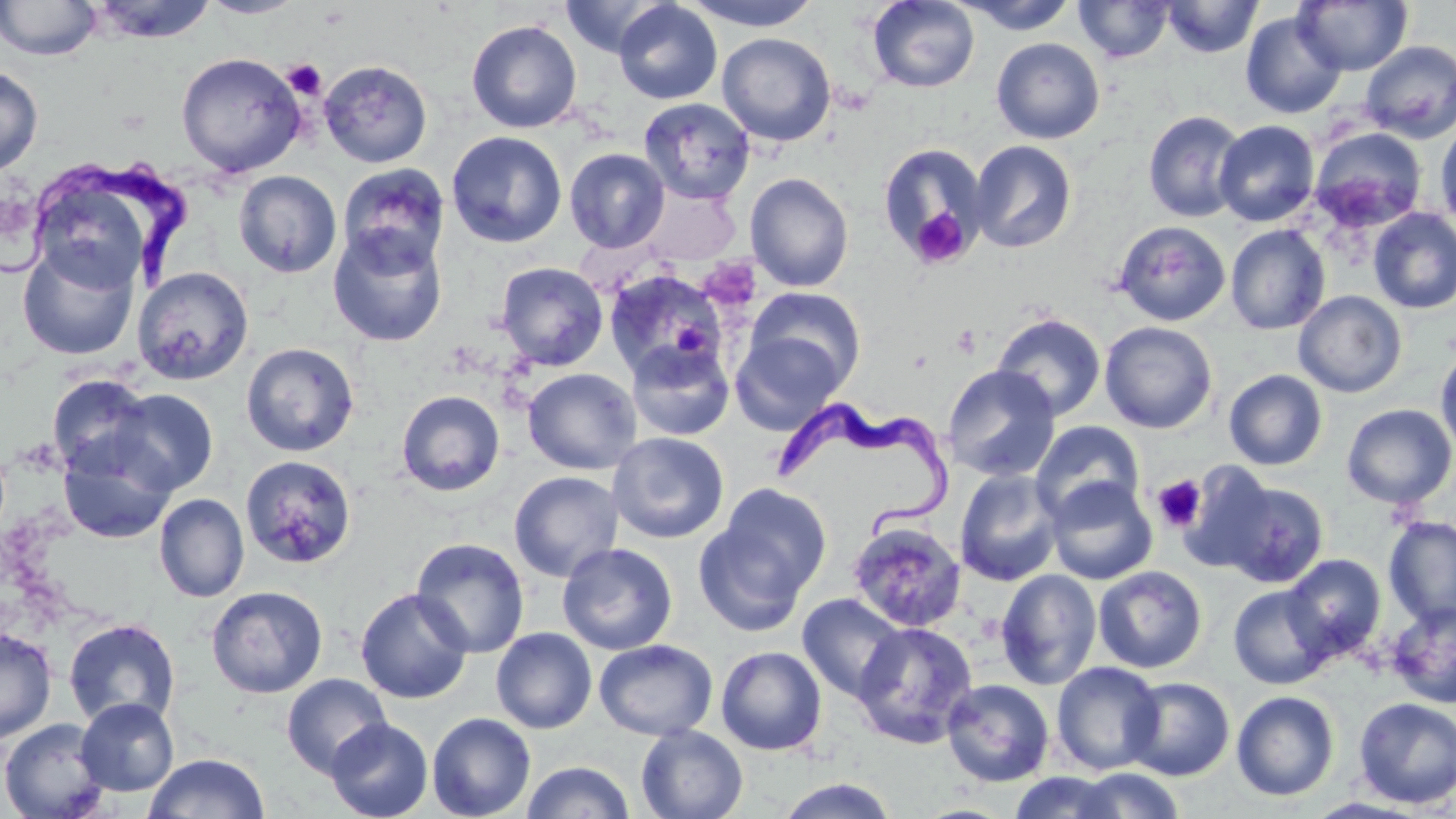
slide-level diagnosis = Trypanosoma brucei
preparation = thin blood smear
Trypanosoma brucei locations = approximate bounding boxes as [x1, y1, x2, y2] in pixels: [8, 159, 193, 293], [778, 400, 952, 542]
uninfected red blood cell locations = approximate bounding boxes as [x1, y1, x2, y2] in pixels: [0, 0, 103, 60], [87, 0, 220, 44], [197, 0, 308, 19], [561, 0, 669, 58], [685, 0, 821, 30], [1074, 0, 1175, 62], [1161, 0, 1262, 58], [614, 1, 723, 105], [867, 1, 980, 93], [952, 1, 1079, 34], [1294, 1, 1412, 74], [1240, 11, 1347, 119], [466, 19, 582, 133], [717, 32, 836, 146], [992, 38, 1105, 143], [983, 40, 1092, 254], [1359, 40, 1456, 144], [176, 52, 306, 177], [318, 59, 433, 168], [0, 66, 43, 176], [639, 97, 756, 203], [1143, 110, 1247, 223], [1213, 119, 1320, 226], [1434, 122, 1456, 230], [1310, 127, 1427, 232], [446, 130, 567, 248], [969, 140, 1077, 253], [877, 143, 989, 263], [564, 148, 670, 253], [337, 163, 450, 272], [233, 170, 342, 278], [745, 172, 854, 292], [639, 183, 740, 264], [1368, 207, 1456, 314], [1113, 220, 1230, 326], [327, 224, 448, 347], [1225, 224, 1330, 335], [17, 240, 140, 361], [495, 262, 608, 371], [132, 266, 254, 385], [604, 270, 727, 380], [745, 287, 866, 394], [1293, 290, 1407, 398], [992, 312, 1106, 421], [1100, 321, 1218, 434], [731, 332, 846, 435], [626, 339, 736, 441], [241, 342, 359, 456], [1434, 344, 1456, 458], [942, 364, 1060, 482], [522, 367, 643, 475], [1224, 369, 1328, 470], [47, 373, 158, 479], [106, 387, 218, 495], [396, 390, 505, 496], [1341, 403, 1456, 509], [1031, 421, 1144, 523], [57, 432, 177, 545], [607, 432, 729, 543], [239, 455, 357, 570], [1176, 463, 1280, 575], [954, 469, 1064, 587], [508, 470, 624, 583], [1046, 478, 1158, 584], [1220, 481, 1329, 588], [715, 485, 831, 600], [154, 493, 249, 602], [1384, 516, 1456, 627], [692, 518, 812, 638], [847, 519, 967, 633], [410, 537, 529, 657], [557, 542, 678, 655], [1281, 554, 1386, 661], [1093, 566, 1207, 673], [995, 569, 1102, 690], [205, 585, 328, 699], [1228, 585, 1334, 689], [354, 587, 474, 704], [797, 593, 908, 702], [1386, 601, 1456, 708], [63, 618, 181, 729], [852, 622, 977, 748], [0, 627, 57, 745], [491, 627, 598, 733], [594, 638, 717, 741], [715, 646, 827, 755], [1052, 661, 1164, 775], [281, 673, 392, 778], [1123, 676, 1235, 781], [942, 679, 1055, 786], [1231, 690, 1340, 801], [75, 698, 179, 796], [1353, 698, 1456, 809], [426, 712, 536, 819], [0, 717, 112, 819], [325, 717, 433, 819], [636, 725, 748, 819], [143, 752, 270, 818], [520, 760, 635, 819], [1065, 767, 1189, 818], [1006, 772, 1127, 818], [775, 777, 900, 819]
modality = optical microscopy
magnification = 1000x
field of view = one of a larger specimen
image size = 1456×819 pixels
stain = May-Grünwald-Giemsa
platelet locations = approximate bounding boxes as [x1, y1, x2, y2] in pixels: [283, 59, 326, 100], [909, 206, 972, 268], [699, 258, 762, 311], [672, 321, 712, 359], [951, 324, 981, 358], [1152, 474, 1207, 533]